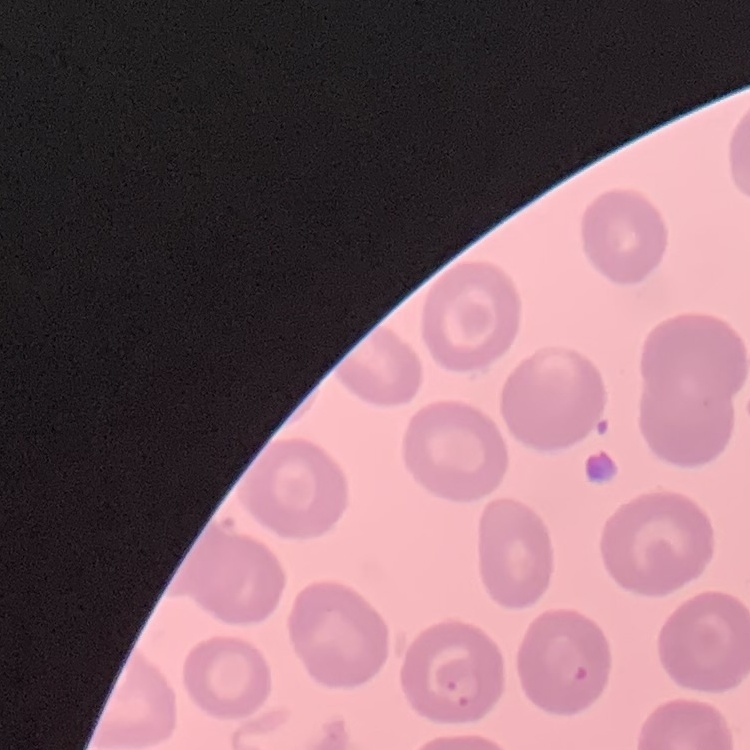 The erythrocytes show no rouleaux formation. Thin peripheral smear. Stained with either Field's or Giemsa. Square crop of a larger photomicrograph.